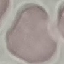

Result: no malaria parasites seen. Cell patch, automatically extracted from a larger field of view and resized to 64 × 64 pixels. Thin blood smear. Giemsa-stained preparation. Acquired by smartphone through the microscope eyepiece.